Locate every leukocyte (white blood cell).
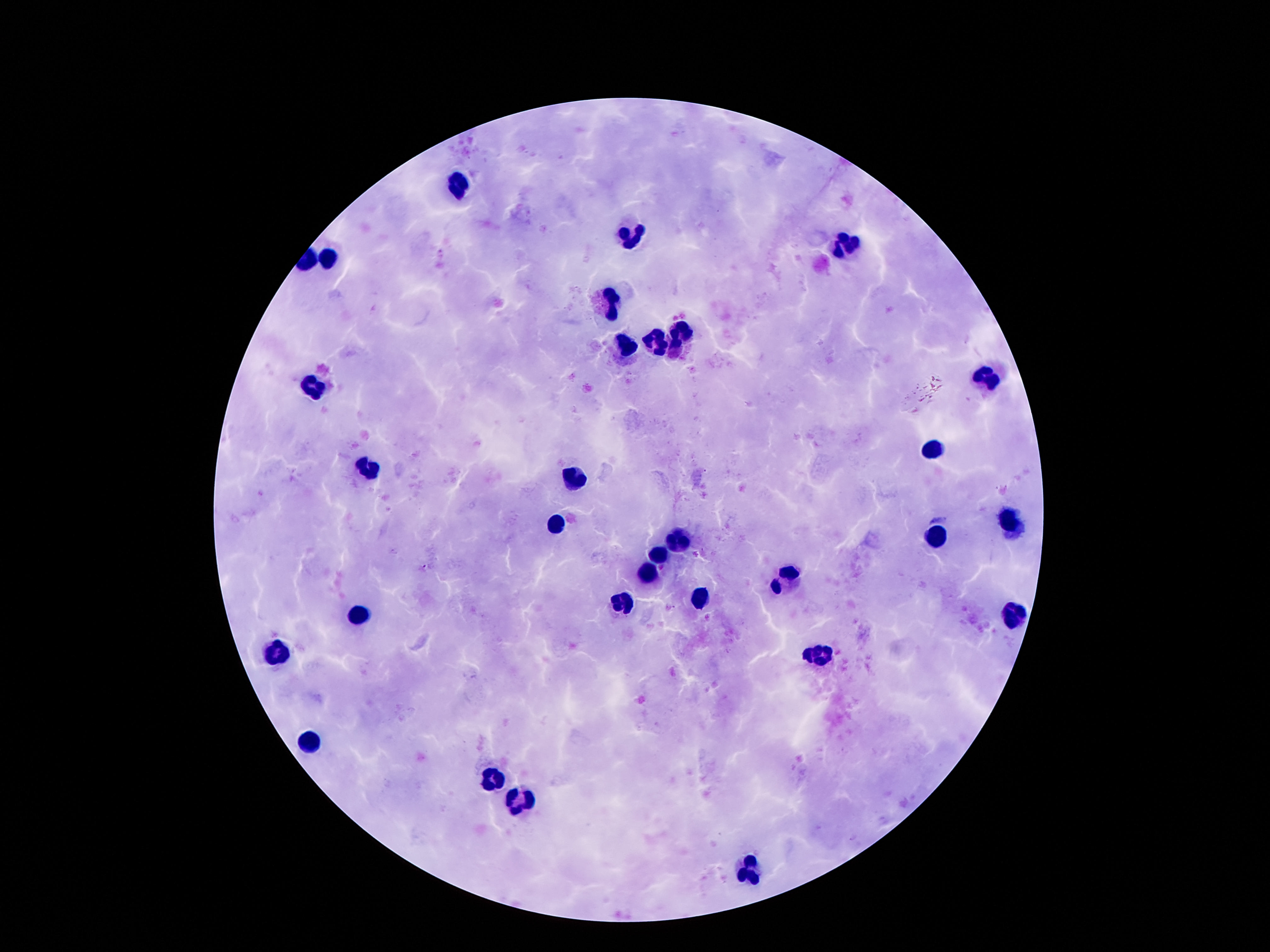
Approximate centers as [x, y] in pixels.
Leukocytes: [459, 183], [631, 237], [847, 244], [330, 259], [612, 306], [683, 335], [659, 340], [629, 346], [988, 378], [316, 387], [935, 447], [372, 467], [575, 479], [1012, 523], [557, 524], [940, 538], [674, 540], [659, 555], [649, 571], [785, 583], [699, 598], [622, 600], [357, 613], [1015, 615], [274, 654], [819, 655], [310, 741], [491, 778], [516, 801], [753, 867].

Smartphone photograph taken through the microscope eyepiece. Image is 1270×952 pixels. One field from this slide. Thick blood film. Giemsa stain. Patient malaria status: uninfected. 100x magnification.